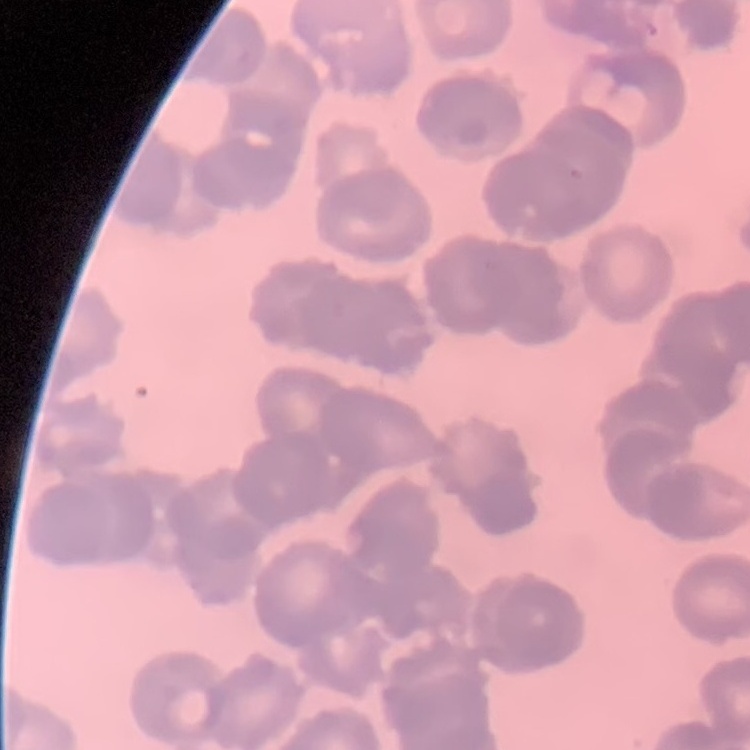

red_blood_cell_morphology: rouleaux formation
image_type: square crop of a larger photomicrograph
stain: Field's or Giemsa
preparation: thin peripheral smear